Assess the morphology of the red blood cells.
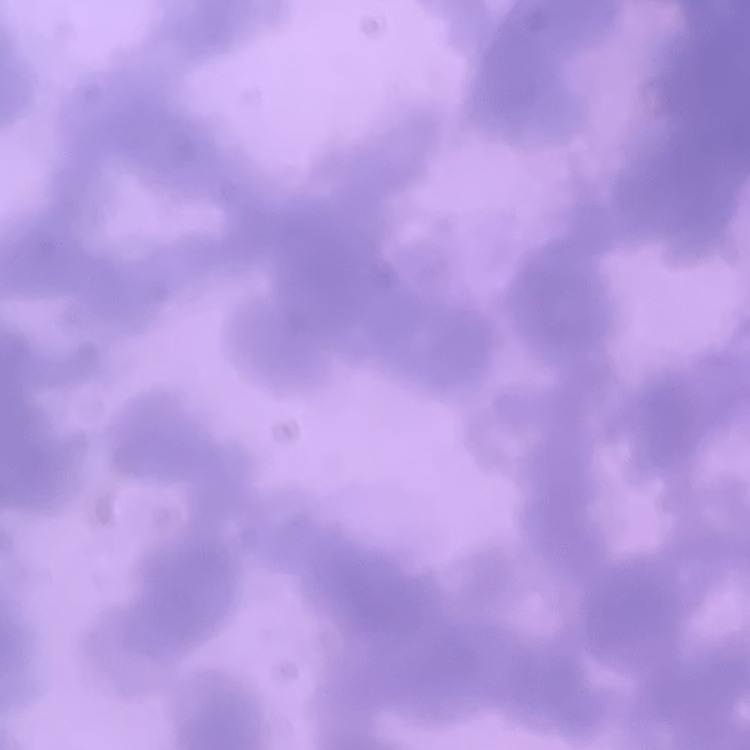
They show rouleaux formation.

preparation: thin peripheral smear
image_type: one tile cut from a larger photomicrograph
stain: Field's or Giemsa